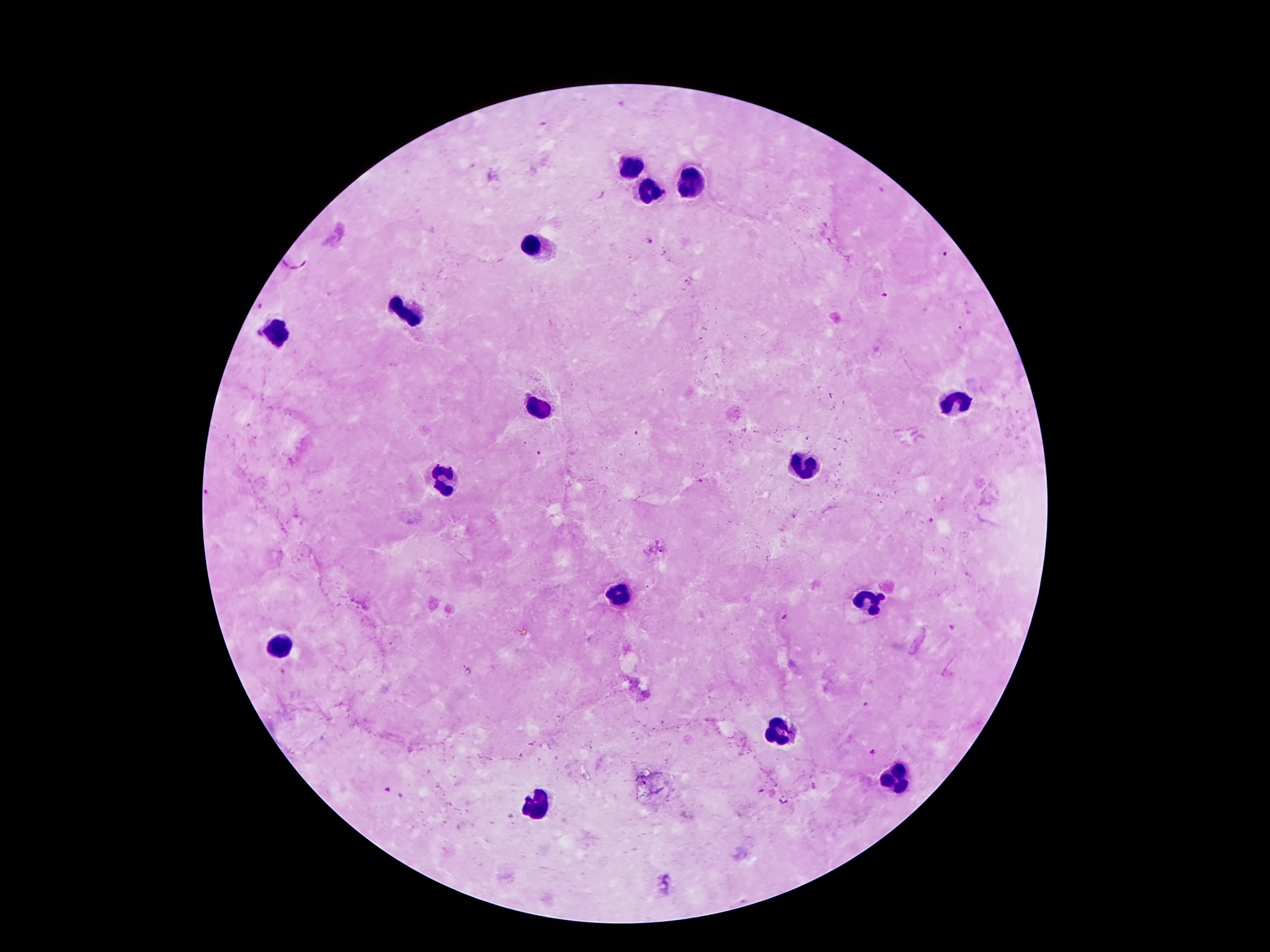

Approximate centers as {x, y} in pixels.
Summary:
  - Plasmodium parasite locations: {650, 241}, {942, 254}, {884, 294}, {636, 433}, {538, 454}, {698, 480}, {932, 521}, {782, 617}, {951, 626}, {865, 704}, {873, 752}, {760, 789}, {386, 790}, {400, 797}
  - Leukocyte locations: {626, 169}, {690, 179}, {653, 191}, {533, 247}, {408, 316}, {279, 333}, {958, 403}, {533, 404}, {805, 465}, {444, 479}, {619, 596}, {869, 604}, {281, 645}, {778, 731}, {899, 783}, {533, 804}
  - Capture: smartphone camera through the microscope eyepiece
  - Magnification: 100x
  - Preparation: thick blood smear
  - Patient malaria status: positive for Plasmodium falciparum
  - Field of view: one from this slide
  - Stain: Giemsa
  - Image size: 1270×952 pixels